Give the position of every malaria parasite.
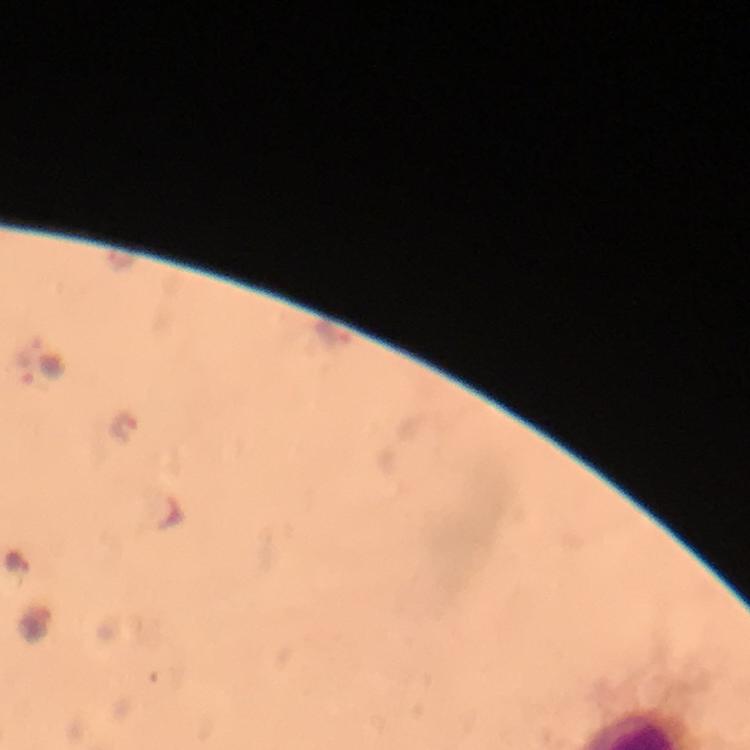
Approximate object centers, in pixels from the top-left corner.
Malaria parasites: (x=335, y=335), (x=22, y=365), (x=125, y=431), (x=16, y=565).

Summary:
  - Capture: smartphone photograph through a microscope
  - Magnification: 100x
  - Context: from a malaria diagnostic workup
  - Immersion oil: used
  - Cropped from: one field of view
  - Image size: 750×750 pixels
  - Stain: Giemsa
  - Preparation: thick blood smear